Locate every Plasmodium parasite.
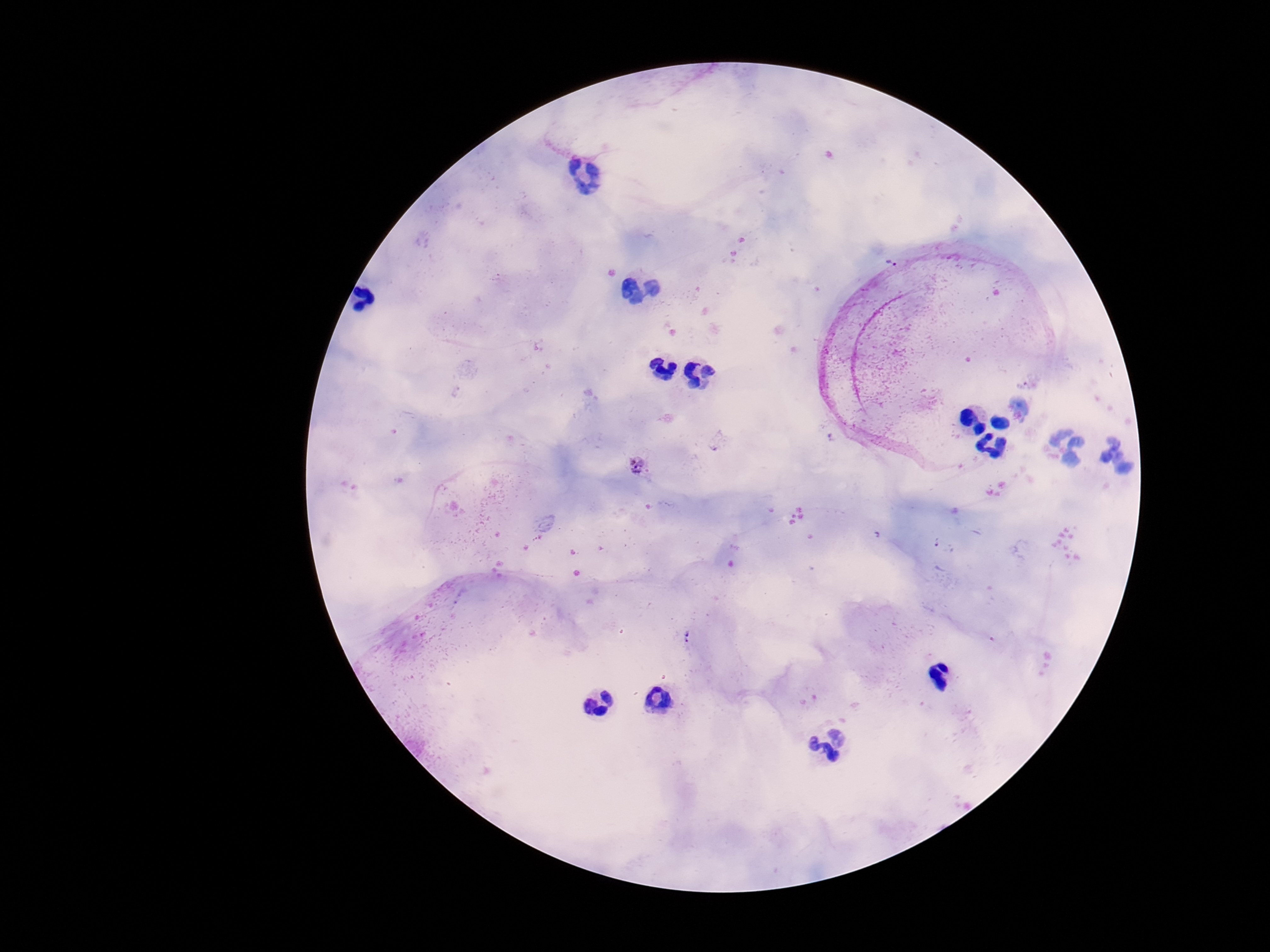
Approximate centers as (x, y) in pixels.
Plasmodium parasites: (893, 261), (638, 467), (688, 639).

Summary:
  - Field of view: single
  - Magnification: 100x
  - Stain: Giemsa
  - Image size: 1270×952 pixels
  - Capture: smartphone camera through the microscope eyepiece
  - Patient malaria status: infected
  - Preparation: thick peripheral-blood smear